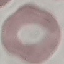 Result: no malaria parasites seen. Thin blood smear. Photographed with a smartphone camera at the microscope eyepiece. Automatically extracted cell patch, resized to 64 × 64 pixels. Giemsa stain.